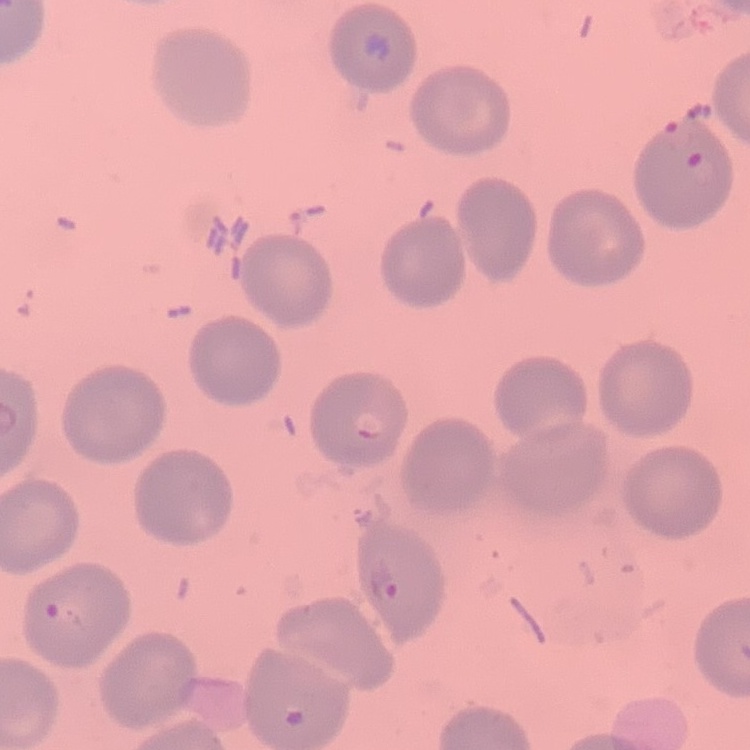
red blood cell morphology = no rouleaux formation
stain = Field's or Giemsa
image type = one tile cut from a larger photomicrograph
preparation = thin peripheral smear